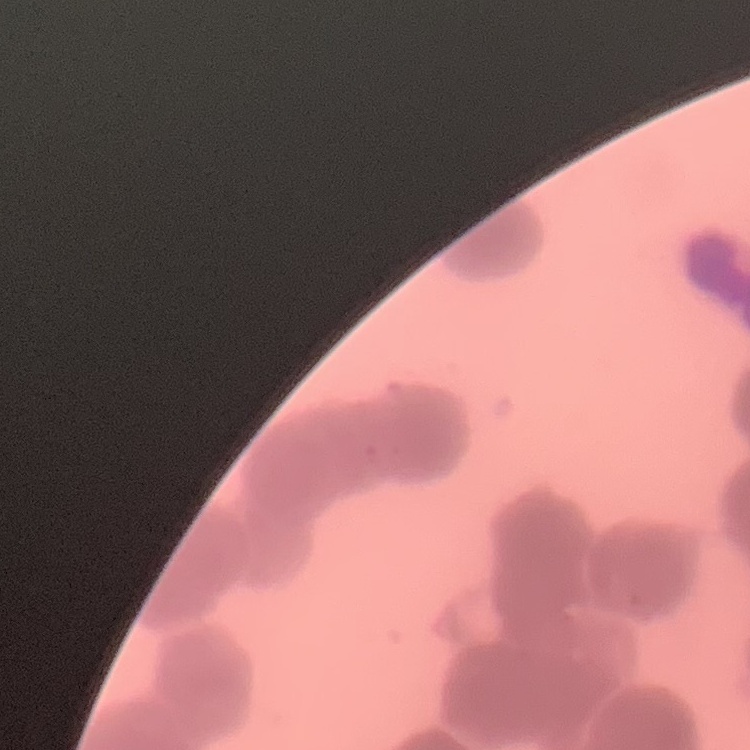
Summary:
  - Red blood cell morphology: rouleaux formation
  - Image type: square crop of a larger photomicrograph
  - Preparation: thin peripheral smear
  - Stain: Field's or Giemsa